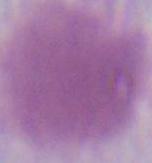 An erythrocyte is shown. Captured at 1000x magnification. Photomicrograph.